Give the position of every leukocyte visible.
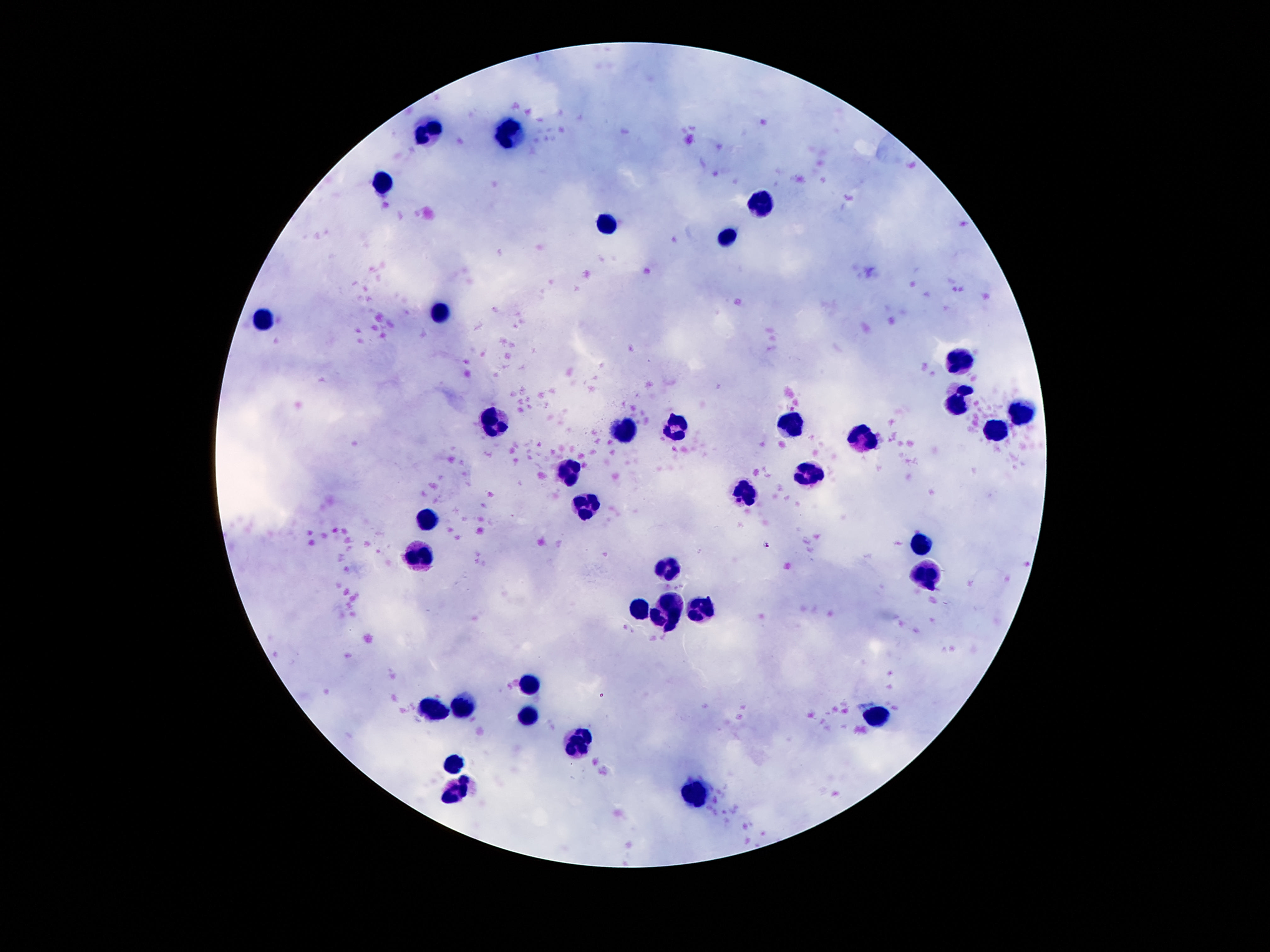
Approximate object centers, in pixels from the top-left corner.
Leukocytes: (x=427, y=132), (x=508, y=135), (x=382, y=183), (x=761, y=207), (x=605, y=222), (x=729, y=237), (x=439, y=312), (x=261, y=318), (x=959, y=360), (x=959, y=398), (x=1025, y=416), (x=492, y=422), (x=676, y=425), (x=792, y=426), (x=989, y=427), (x=622, y=430), (x=861, y=440), (x=569, y=472), (x=808, y=472), (x=746, y=495), (x=581, y=508), (x=429, y=519), (x=917, y=545), (x=422, y=556), (x=670, y=570), (x=927, y=573), (x=671, y=598), (x=635, y=608), (x=698, y=608), (x=657, y=620), (x=531, y=685), (x=466, y=703), (x=431, y=710), (x=529, y=713), (x=882, y=717), (x=578, y=744), (x=455, y=765), (x=459, y=792), (x=696, y=795).

{
  "capture": "smartphone camera through the microscope eyepiece",
  "patient_malaria_status": "uninfected",
  "image_size": "1270×952 pixels",
  "preparation": "thick blood smear",
  "stain": "Giemsa",
  "magnification": "100x",
  "field_of_view": "single"
}